Name the cell type shown.
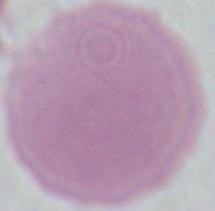

An erythrocyte.

magnification = 1000x
modality = micrograph